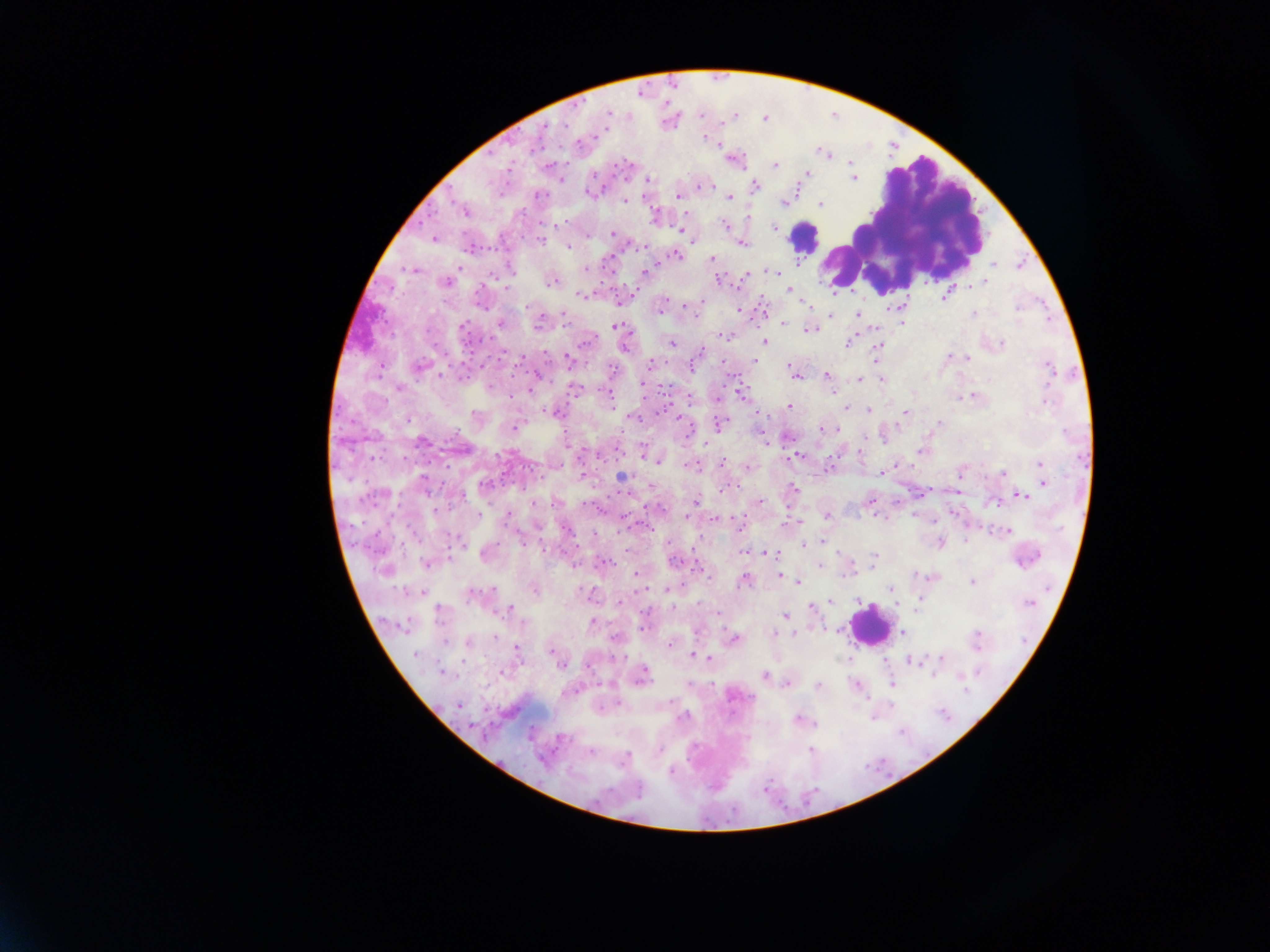 Approximate centers as (x, y) in pixels. Plasmodium parasite locations: (608, 112), (565, 124), (545, 125), (704, 137), (579, 144), (850, 162), (775, 165), (806, 173), (593, 176), (853, 178), (561, 180), (648, 180), (755, 185), (700, 186), (704, 186), (589, 193), (540, 196), (678, 196), (729, 197), (625, 200), (783, 203), (821, 205), (464, 211), (655, 216), (724, 225), (774, 226), (681, 230), (613, 233), (434, 239), (541, 241), (743, 245), (570, 247), (677, 256), (712, 260), (994, 265), (459, 267), (510, 269), (585, 269), (411, 270), (770, 270), (645, 271), (717, 280), (553, 282), (986, 282), (446, 283), (507, 288), (789, 290), (580, 294), (945, 297), (805, 302), (526, 307), (661, 307), (1017, 308), (739, 309), (857, 314), (974, 315), (830, 316), (499, 323), (539, 323), (783, 323), (903, 323), (615, 325), (463, 327), (809, 330), (723, 334), (585, 342), (671, 342), (764, 342), (847, 343), (1002, 344), (624, 346), (878, 347), (950, 356), (967, 358), (876, 359), (521, 360), (755, 360), (568, 361), (649, 364), (722, 364), (692, 365), (420, 366), (789, 368), (1049, 369), (793, 373), (441, 376), (827, 376), (537, 377), (882, 379), (860, 380), (643, 385), (490, 387), (399, 388), (573, 389), (528, 390), (741, 394), (972, 396), (717, 397), (1046, 401), (788, 406), (846, 409), (869, 411), (553, 413), (905, 413), (475, 415), (635, 417), (679, 419), (408, 420), (720, 423), (940, 423), (514, 428), (821, 428), (837, 430), (1067, 432), (884, 438), (422, 441), (765, 443), (644, 451), (921, 451), (797, 456), (656, 462), (722, 462), (896, 464), (1040, 464), (691, 466), (749, 467), (1003, 473), (581, 474), (882, 474), (960, 475), (622, 477), (424, 478), (1044, 483), (484, 484), (793, 488), (726, 490), (1022, 495), (462, 497), (871, 500), (696, 501), (761, 501), (996, 503), (479, 514), (507, 516), (687, 516), (827, 516), (716, 519), (798, 522), (787, 524), (1008, 532), (520, 539), (822, 541), (965, 541), (460, 543), (940, 543), (804, 545), (744, 552), (769, 553), (838, 553), (873, 557), (606, 562), (673, 562), (427, 564), (819, 565), (576, 566), (700, 569), (851, 571), (636, 574), (915, 574), (780, 576), (744, 580), (797, 581), (971, 582), (891, 588), (666, 589), (535, 590), (473, 595), (919, 599), (859, 600), (830, 601), (1029, 603), (812, 607), (673, 608), (510, 609), (439, 615), (785, 617), (592, 622), (903, 631), (773, 634), (977, 636), (495, 638), (734, 638), (445, 641), (468, 643), (669, 644), (516, 649), (550, 651), (416, 654), (693, 655), (709, 658), (941, 658), (912, 662), (560, 664), (502, 672), (442, 673), (764, 675), (934, 675), (643, 676), (688, 683), (787, 683), (892, 683), (853, 684), (818, 685), (966, 690), (565, 692), (459, 706), (683, 717), (797, 719), (561, 739), (811, 750), (590, 752), (627, 757), (671, 772). Leukocyte locations: (902, 221), (804, 237), (869, 626). Photographed through a microscope with a mobile-phone camera. Sample from Ghana. Thick blood film. Image is 1270×952 pixels. Single field of view.